State the blood parasite species.
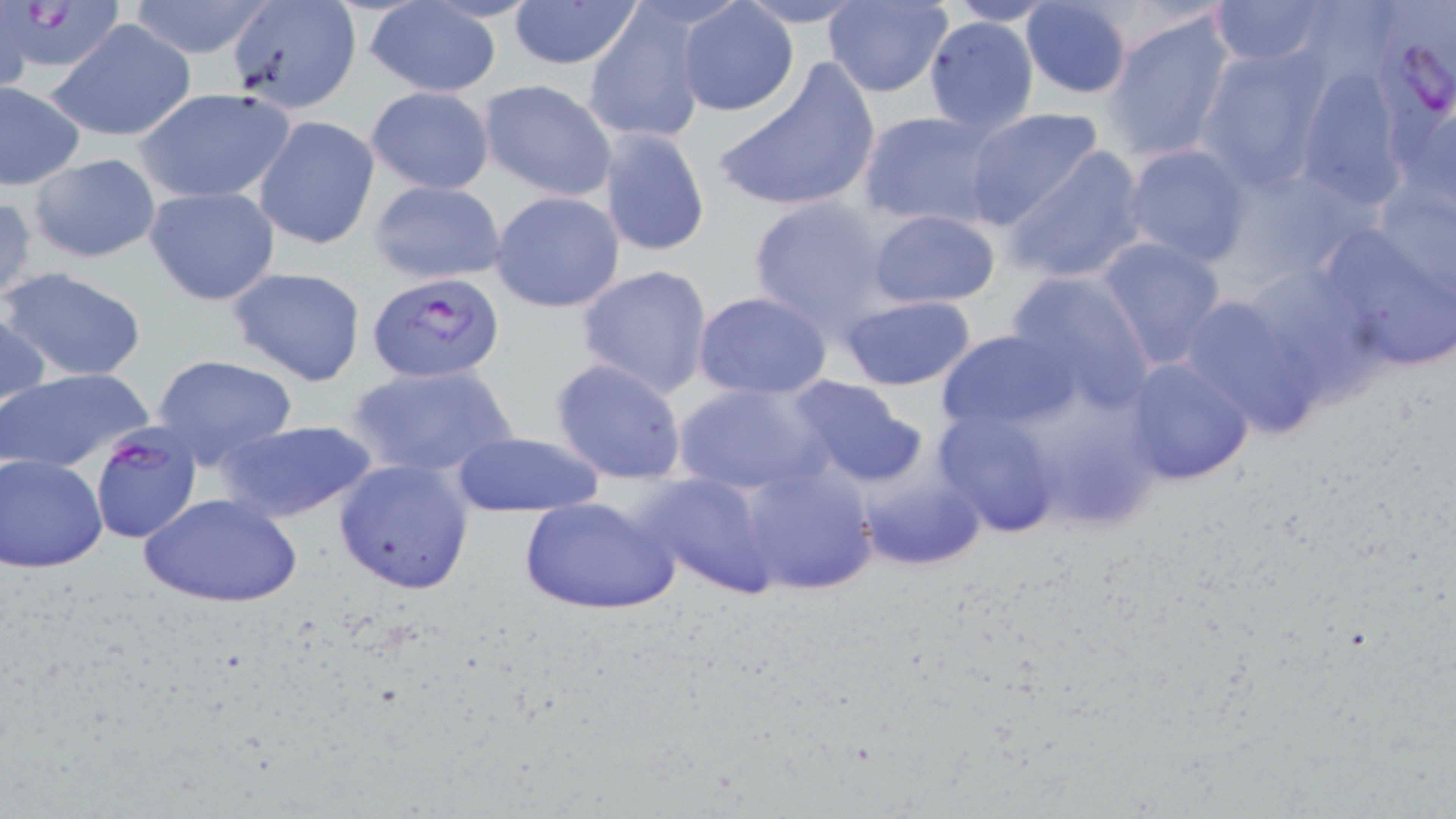
Plasmodium falciparum.

Approximate bounding boxes as [x1, y1, x2, y2] in pixels. Uninfected red blood cell locations: [127, 0, 276, 60], [507, 0, 643, 72], [225, 1, 363, 114], [733, 1, 871, 27], [824, 1, 952, 98], [943, 1, 1057, 26], [1018, 1, 1134, 98], [1207, 1, 1344, 68], [362, 2, 504, 98], [0, 4, 33, 93], [678, 4, 798, 115], [582, 6, 708, 146], [1101, 8, 1238, 165], [922, 15, 1040, 136], [48, 18, 197, 143], [1196, 47, 1336, 186], [708, 59, 883, 216], [1293, 64, 1413, 208], [479, 79, 617, 201], [0, 80, 85, 190], [132, 86, 296, 203], [365, 86, 495, 196], [1388, 94, 1456, 210], [963, 107, 1106, 232], [857, 109, 1003, 230], [254, 115, 380, 251], [597, 128, 711, 258], [1120, 143, 1254, 268], [1005, 147, 1150, 283], [27, 153, 161, 265], [1366, 178, 1453, 302], [368, 179, 509, 285], [144, 186, 280, 307], [489, 190, 625, 314], [0, 195, 37, 305], [747, 195, 899, 333], [867, 207, 1001, 309], [1319, 227, 1456, 371], [1091, 236, 1229, 369], [1240, 258, 1391, 396], [574, 264, 716, 399], [2, 266, 148, 383], [226, 266, 368, 387], [1005, 269, 1157, 407], [693, 290, 835, 401], [1174, 290, 1336, 441], [838, 294, 978, 391], [0, 303, 50, 419], [935, 329, 1075, 436], [150, 355, 300, 469], [550, 357, 690, 484], [1122, 357, 1256, 486], [345, 362, 520, 481], [1, 366, 155, 473], [787, 377, 927, 490], [674, 380, 830, 495], [936, 409, 1063, 536], [213, 419, 379, 525], [451, 432, 605, 518], [1, 454, 107, 573], [333, 458, 476, 595], [736, 459, 881, 598], [853, 460, 990, 572], [634, 472, 781, 601], [139, 490, 303, 608], [517, 494, 681, 617]. Plasmodium falciparum-infected red blood cell locations: [1388, 2, 1455, 134], [4, 3, 123, 81], [368, 271, 503, 383], [89, 424, 203, 544]. Optical microscopy. Thin blood smear. Image is 1456×819 pixels. Single field of view. Captured at 1000x magnification. May-Grünwald-Giemsa-stained preparation.